Assess this cell for malaria.
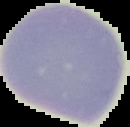

It is uninfected.

image type = segmented cell region on a black background
preparation = thin blood smear
image size = 130×127 pixels